Locate and identify every blood parasite.
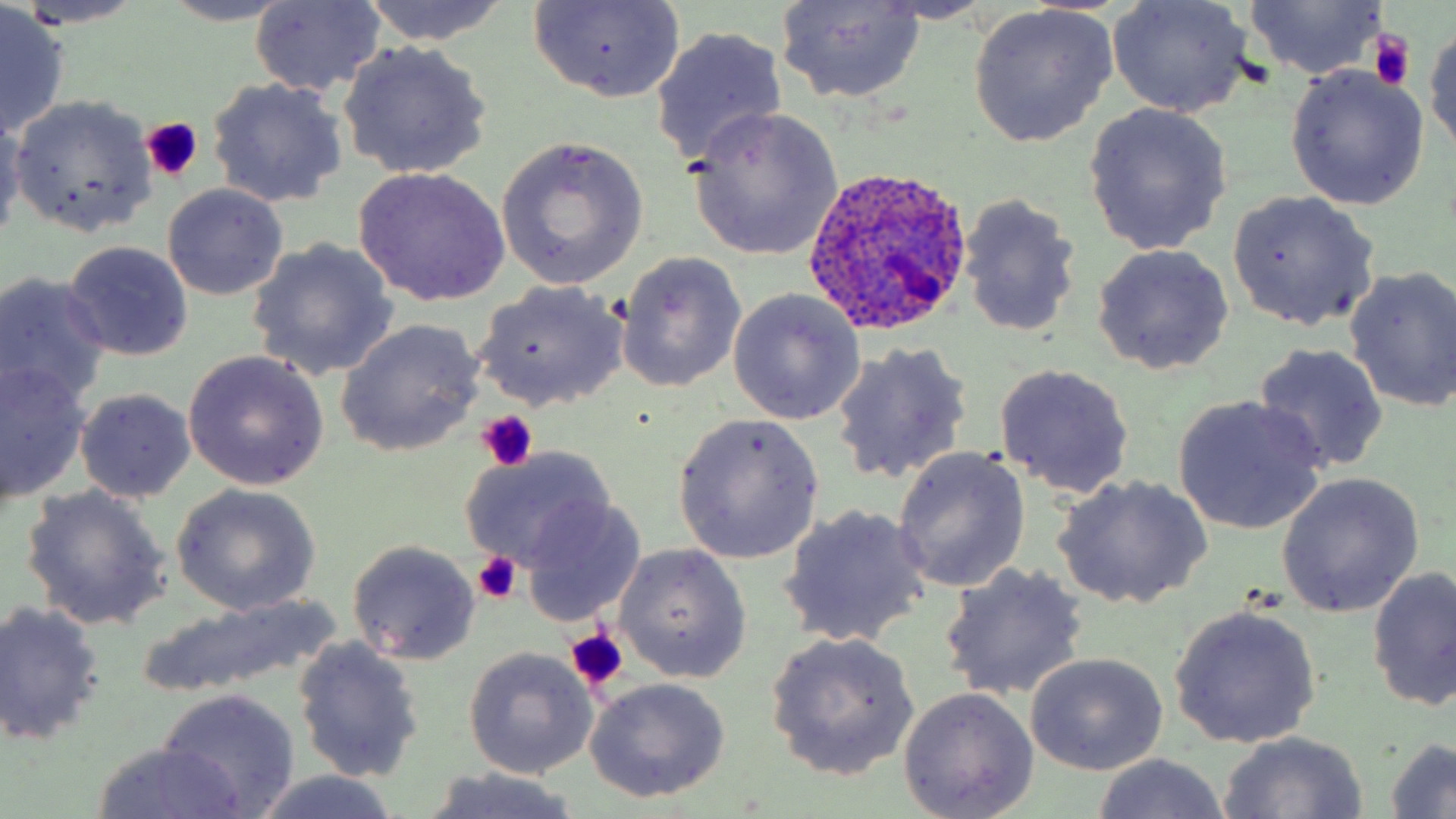
Approximate bounding boxes as named x1/y1/x2/y2 corners in pixels.
Plasmodium ovale-infected red blood cells: (x1=802, y1=163, x2=974, y2=334).
No Plasmodium falciparum, Plasmodium malariae, Plasmodium vivax, Babesia divergens, or Trypanosoma brucei observed.

slide-level diagnosis = Plasmodium ovale
stain = May-Grünwald-Giemsa
magnification = 1000x
preparation = thin blood film
image size = 1456×819 pixels
modality = light microscopy
platelet locations = approximate bounding boxes as named x1/y1/x2/y2 corners in pixels: (x1=1368, y1=30, x2=1417, y2=91), (x1=139, y1=118, x2=203, y2=184), (x1=474, y1=410, x2=538, y2=475), (x1=471, y1=552, x2=524, y2=606), (x1=565, y1=628, x2=627, y2=694)
uninfected red blood cell locations = approximate bounding boxes as named x1/y1/x2/y2 corners in pixels: (x1=9, y1=0, x2=149, y2=29), (x1=355, y1=0, x2=515, y2=48), (x1=1105, y1=0, x2=1254, y2=118), (x1=155, y1=1, x2=300, y2=26), (x1=526, y1=1, x2=686, y2=104), (x1=774, y1=1, x2=928, y2=103), (x1=1241, y1=2, x2=1390, y2=79), (x1=1, y1=3, x2=69, y2=140), (x1=250, y1=3, x2=385, y2=96), (x1=969, y1=4, x2=1117, y2=147), (x1=651, y1=25, x2=788, y2=166), (x1=1426, y1=25, x2=1456, y2=156), (x1=336, y1=42, x2=493, y2=179), (x1=1284, y1=65, x2=1429, y2=208), (x1=208, y1=78, x2=347, y2=206), (x1=9, y1=95, x2=156, y2=235), (x1=1083, y1=103, x2=1233, y2=255), (x1=685, y1=107, x2=843, y2=262), (x1=0, y1=112, x2=28, y2=242), (x1=497, y1=136, x2=649, y2=290), (x1=351, y1=166, x2=511, y2=306), (x1=162, y1=183, x2=289, y2=301), (x1=1225, y1=189, x2=1381, y2=332), (x1=957, y1=193, x2=1084, y2=342), (x1=245, y1=238, x2=399, y2=382), (x1=64, y1=240, x2=193, y2=362), (x1=1091, y1=244, x2=1235, y2=375), (x1=615, y1=251, x2=749, y2=391), (x1=1345, y1=265, x2=1456, y2=414), (x1=0, y1=272, x2=110, y2=409), (x1=475, y1=281, x2=629, y2=411), (x1=727, y1=289, x2=864, y2=424), (x1=335, y1=320, x2=485, y2=457), (x1=831, y1=341, x2=974, y2=487), (x1=1250, y1=344, x2=1390, y2=473), (x1=183, y1=351, x2=330, y2=491), (x1=0, y1=362, x2=90, y2=503), (x1=994, y1=363, x2=1135, y2=497), (x1=74, y1=389, x2=197, y2=503), (x1=1172, y1=396, x2=1328, y2=534), (x1=672, y1=413, x2=825, y2=564), (x1=892, y1=446, x2=1030, y2=594), (x1=458, y1=448, x2=618, y2=573), (x1=1275, y1=471, x2=1426, y2=619), (x1=1053, y1=475, x2=1211, y2=610), (x1=169, y1=483, x2=322, y2=615), (x1=21, y1=484, x2=173, y2=632), (x1=518, y1=498, x2=646, y2=626), (x1=776, y1=504, x2=932, y2=646), (x1=347, y1=540, x2=481, y2=665), (x1=614, y1=545, x2=751, y2=682), (x1=938, y1=562, x2=1091, y2=703), (x1=1367, y1=566, x2=1456, y2=711), (x1=138, y1=590, x2=340, y2=701), (x1=0, y1=601, x2=105, y2=745), (x1=1169, y1=604, x2=1322, y2=748), (x1=766, y1=632, x2=921, y2=782), (x1=292, y1=636, x2=425, y2=783), (x1=464, y1=647, x2=597, y2=778), (x1=1024, y1=652, x2=1169, y2=775), (x1=586, y1=677, x2=732, y2=803), (x1=899, y1=688, x2=1039, y2=818), (x1=159, y1=689, x2=300, y2=816), (x1=1218, y1=731, x2=1368, y2=816), (x1=1383, y1=738, x2=1455, y2=817), (x1=89, y1=741, x2=249, y2=818), (x1=1089, y1=754, x2=1233, y2=819), (x1=419, y1=769, x2=590, y2=819), (x1=249, y1=773, x2=406, y2=819)
field of view = single